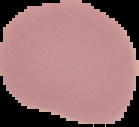

Image is 139×127 pixels. From a thin blood smear. Cell region segmented out of the field of view; the surrounding area is masked to black. Result: negative for Plasmodium parasites.